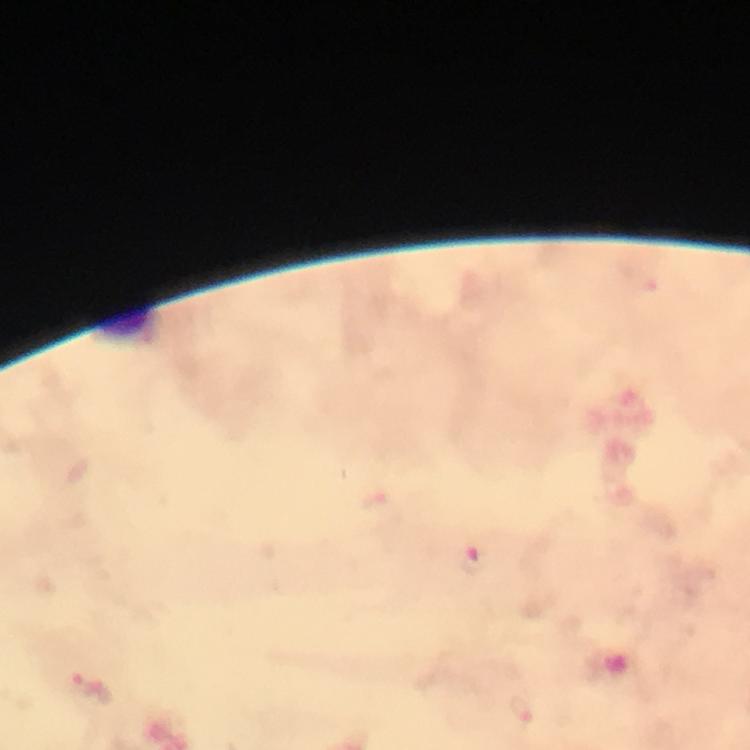 Approximate object centers, in pixels from the top-left corner. Malaria parasite locations: (x=475, y=564). Photographed with a smartphone mounted on the microscope. At 100x magnification. Giemsa-stained preparation. Cropped region of a single field of view. Immersion oil applied. From a malaria diagnostic workup. Thick blood film. Image is 750×750 pixels.